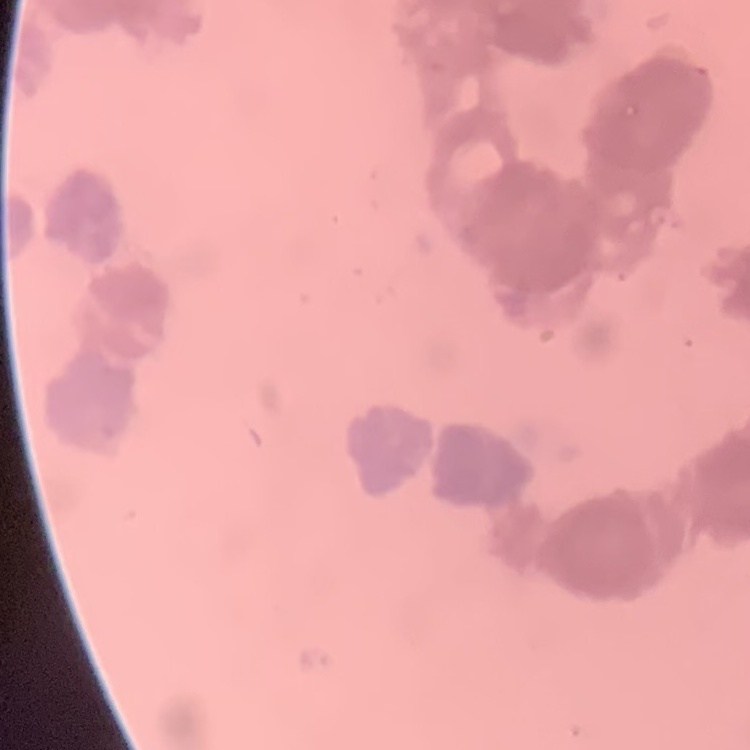

erythrocyte_morphology: rouleaux formation
preparation: thin blood film
image_type: square crop of a larger photomicrograph
stain: Field's or Giemsa